Name the cell type shown.
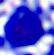

A leukocyte.

modality = micrograph
magnification = 400x